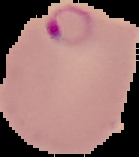
Cell region segmented out of the field of view; the surrounding area is masked to black. From a thin blood film. Image is 139×157 pixels. Result: Plasmodium parasites identified.